Point out each malaria parasite.
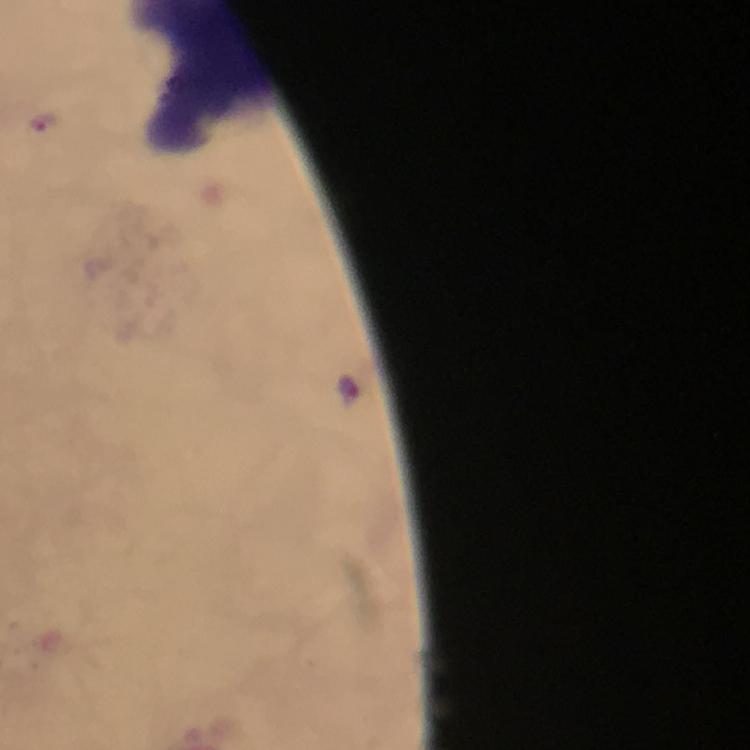

Approximate centers as (x, y) in pixels.
Malaria parasites: (47, 123), (348, 389).

capture = smartphone photograph through a microscope
cropped from = one field of view
immersion oil = applied
preparation = thick smear
magnification = 100x
stain = Giemsa
image size = 750×750 pixels
context = from a diagnostic examination for malaria